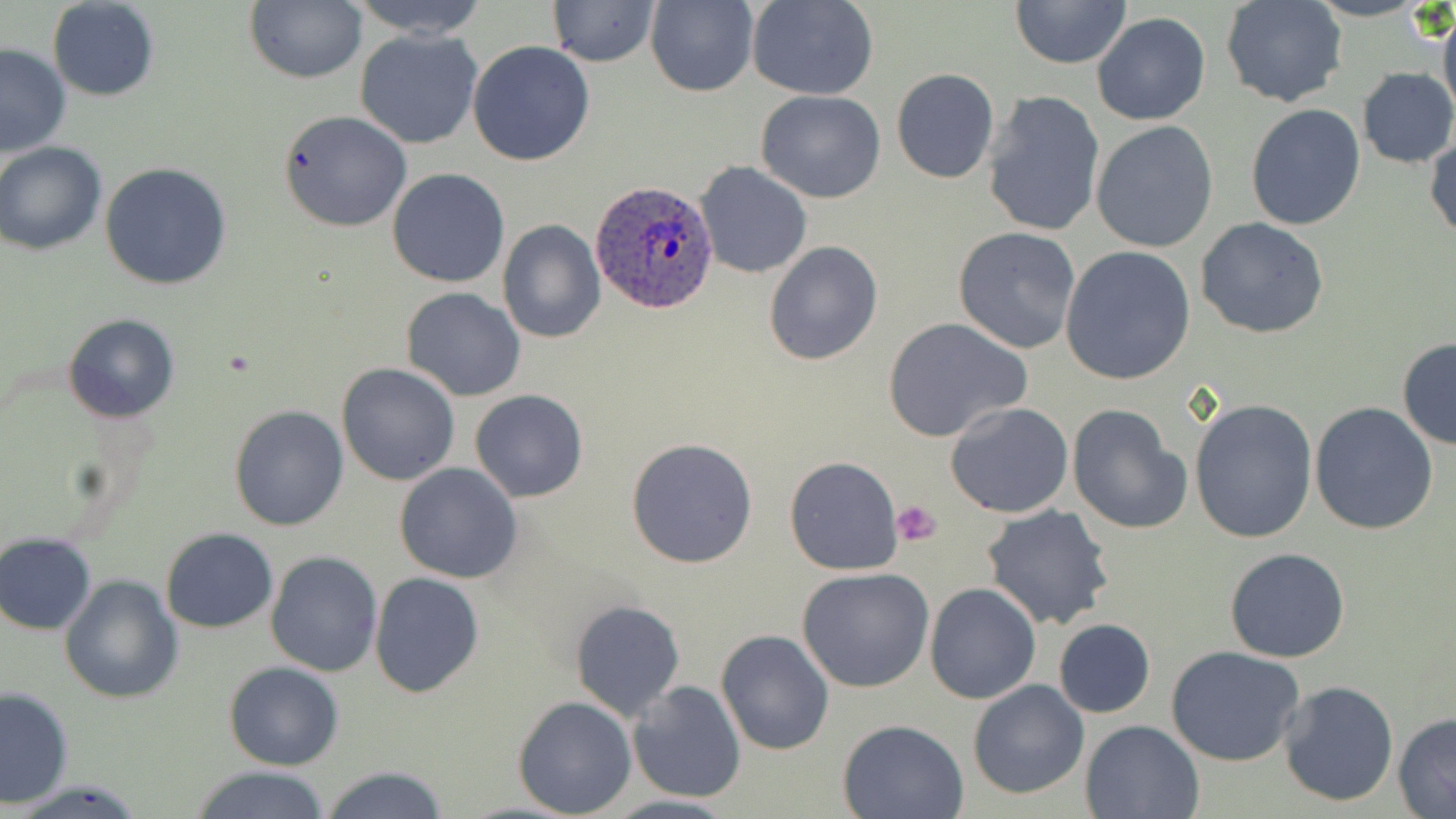
Approximate bounding boxes as [x1, y1, x2, y2] in pixels. Platelet locations: [891, 501, 942, 546]. Plasmodium ovale-infected red blood cell locations: [588, 180, 720, 316]. Uninfected red blood cell locations: [47, 0, 160, 101], [348, 0, 491, 38], [548, 0, 661, 66], [748, 0, 877, 100], [245, 1, 366, 84], [644, 1, 759, 97], [1009, 1, 1132, 70], [1222, 1, 1347, 108], [1438, 1, 1456, 125], [1091, 11, 1211, 126], [355, 29, 483, 149], [466, 41, 596, 167], [0, 44, 71, 157], [892, 67, 1000, 183], [1356, 67, 1456, 168], [983, 90, 1105, 237], [756, 91, 885, 204], [1245, 103, 1366, 231], [279, 109, 412, 232], [1091, 120, 1219, 253], [1426, 132, 1456, 242], [0, 141, 109, 255], [695, 161, 812, 279], [99, 162, 232, 290], [387, 168, 509, 288], [1195, 218, 1329, 339], [498, 220, 605, 342], [952, 227, 1082, 355], [764, 241, 882, 366], [1060, 246, 1197, 385], [401, 287, 527, 401], [64, 315, 179, 422], [882, 317, 1032, 441], [1396, 338, 1456, 450], [335, 363, 459, 485], [470, 389, 587, 503], [1188, 398, 1319, 544], [945, 402, 1075, 517], [1068, 403, 1193, 534], [1310, 403, 1439, 536], [228, 405, 348, 531], [625, 437, 758, 569], [785, 455, 904, 574], [394, 463, 523, 584], [981, 503, 1115, 630], [161, 528, 277, 632], [1, 533, 97, 634], [1225, 548, 1351, 662], [265, 552, 382, 677], [796, 569, 935, 693], [370, 572, 483, 697], [60, 574, 182, 703], [926, 582, 1041, 704], [572, 600, 684, 720], [1054, 619, 1156, 718], [716, 630, 833, 755], [1166, 644, 1307, 768], [225, 661, 344, 769], [1278, 679, 1398, 808], [968, 680, 1090, 800], [628, 682, 745, 802], [1, 686, 75, 809], [513, 696, 637, 817], [1393, 711, 1456, 819], [838, 718, 969, 818], [1080, 719, 1205, 818], [189, 764, 332, 819], [319, 765, 449, 819], [604, 794, 741, 818]. Slide-level diagnosis: Plasmodium ovale. May-Grünwald-Giemsa stain. Single field of view. Thin blood smear. Optical microscopy. 1000x magnification. Image is 1456×819 pixels.